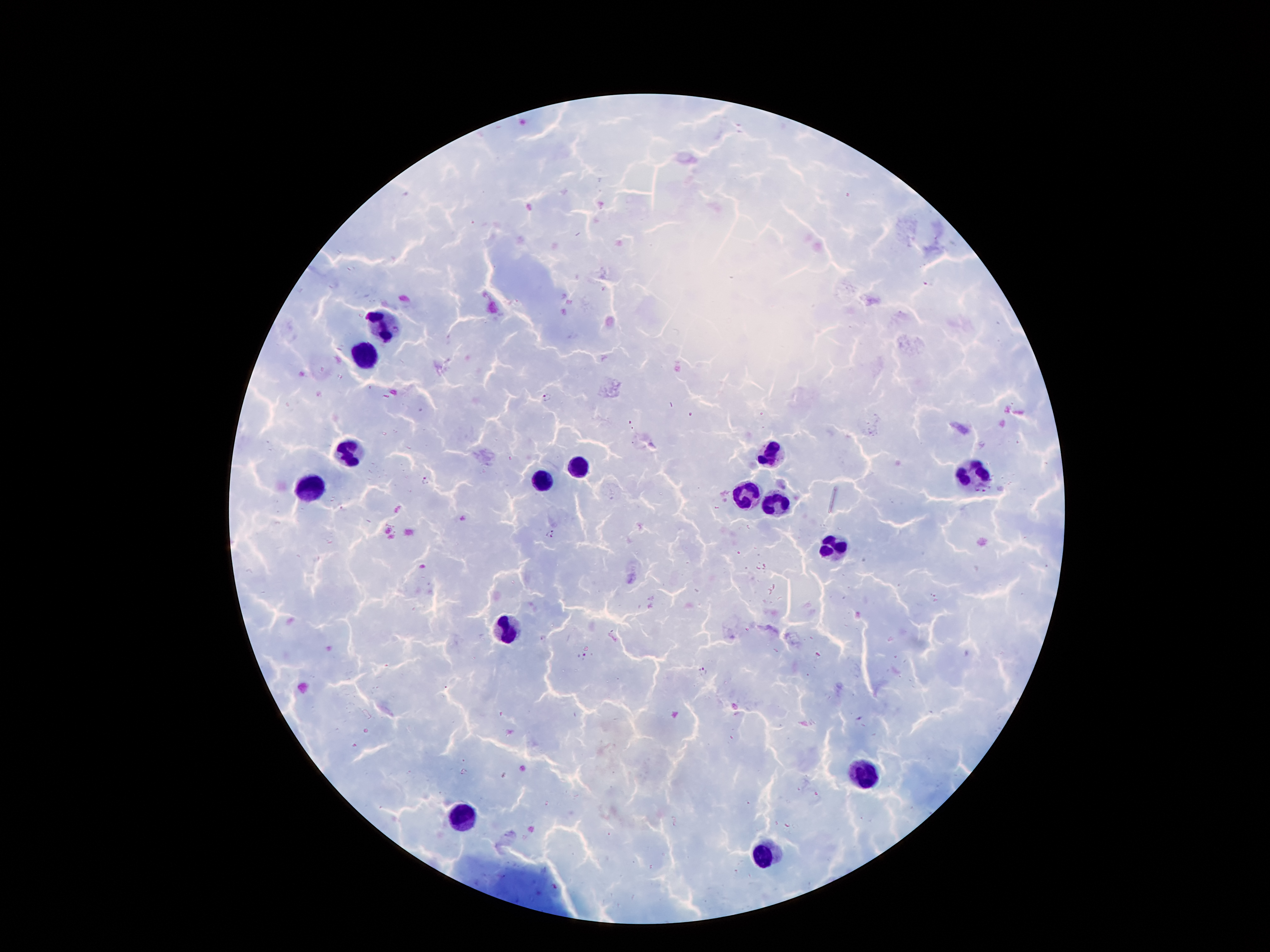
Approximate object centers, in pixels from the top-left corner.
Summary:
  - Malaria parasite locations: (x=929, y=282), (x=548, y=397), (x=426, y=480), (x=975, y=489), (x=987, y=490), (x=547, y=528), (x=552, y=538), (x=582, y=657), (x=703, y=671)
  - Leukocyte locations: (x=385, y=323), (x=364, y=357), (x=348, y=451), (x=768, y=454), (x=572, y=466), (x=971, y=472), (x=539, y=481), (x=312, y=487), (x=746, y=496), (x=776, y=502), (x=833, y=548), (x=509, y=628), (x=864, y=773), (x=465, y=817), (x=765, y=853)
  - Magnification: 100x
  - Stain: Giemsa
  - Preparation: thick blood smear
  - Image size: 1270×952 pixels
  - Capture: smartphone through the microscope eyepiece
  - Field of view: single
  - Patient malaria status: positive for Plasmodium falciparum